Assess the morphology of the erythrocytes.
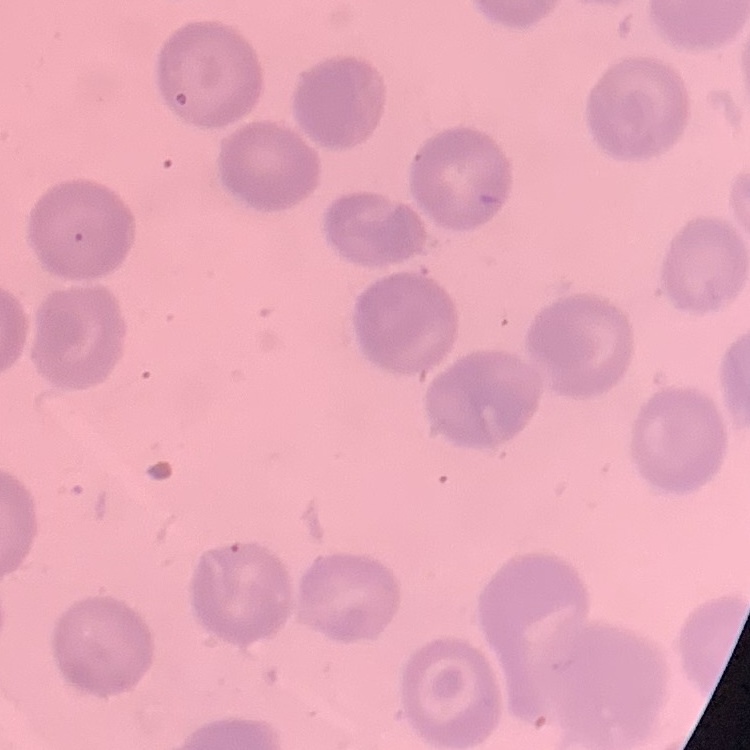
No rouleaux formation.

Stained with either Field's or Giemsa. Square crop of a larger photomicrograph. Thin blood film.